Report the malaria status of this cell.
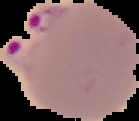

Parasitized.

{
  "image_type": "cell region segmented out of the field of view; surrounding area masked to black",
  "image_size": "139×121 pixels",
  "preparation": "thin blood film"
}